Give a bounding box for every leukocyte visible.
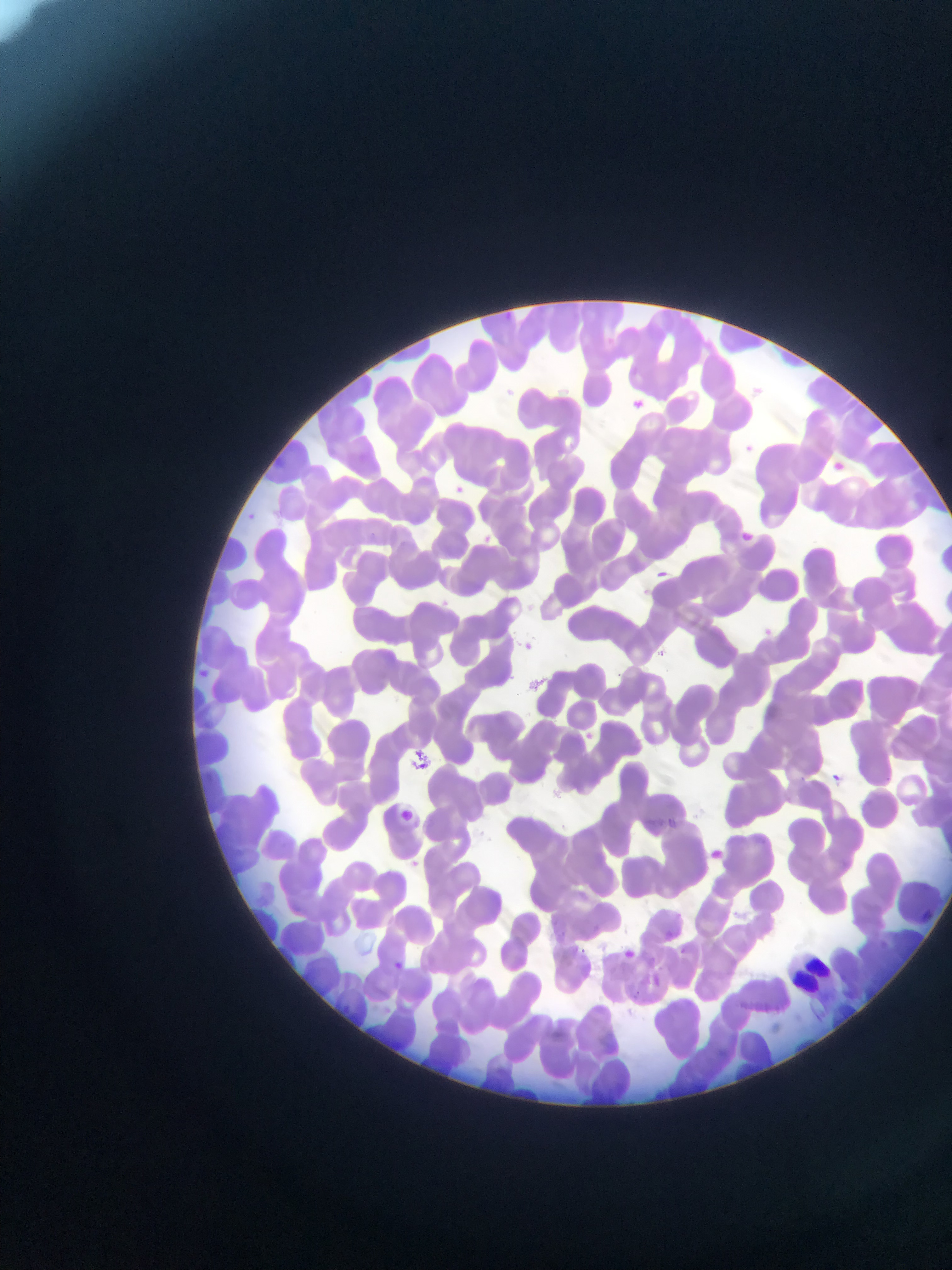

Approximate bounding boxes as left top right bottom in pixels.
Leukocytes: 785 947 839 995.

Summary:
  - Country: Ghana
  - Field of view: single
  - Capture: mobile-phone photograph through a microscope
  - Image size: 952×1270 pixels
  - Preparation: thin blood film